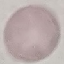
Result: negative for malaria parasites. Thin smear of blood. Giemsa stain. Photographed with a smartphone camera at the microscope eyepiece. Cell patch, automatically extracted from a larger field of view and resized to 64 × 64 pixels.